Locate and identify every blood parasite.
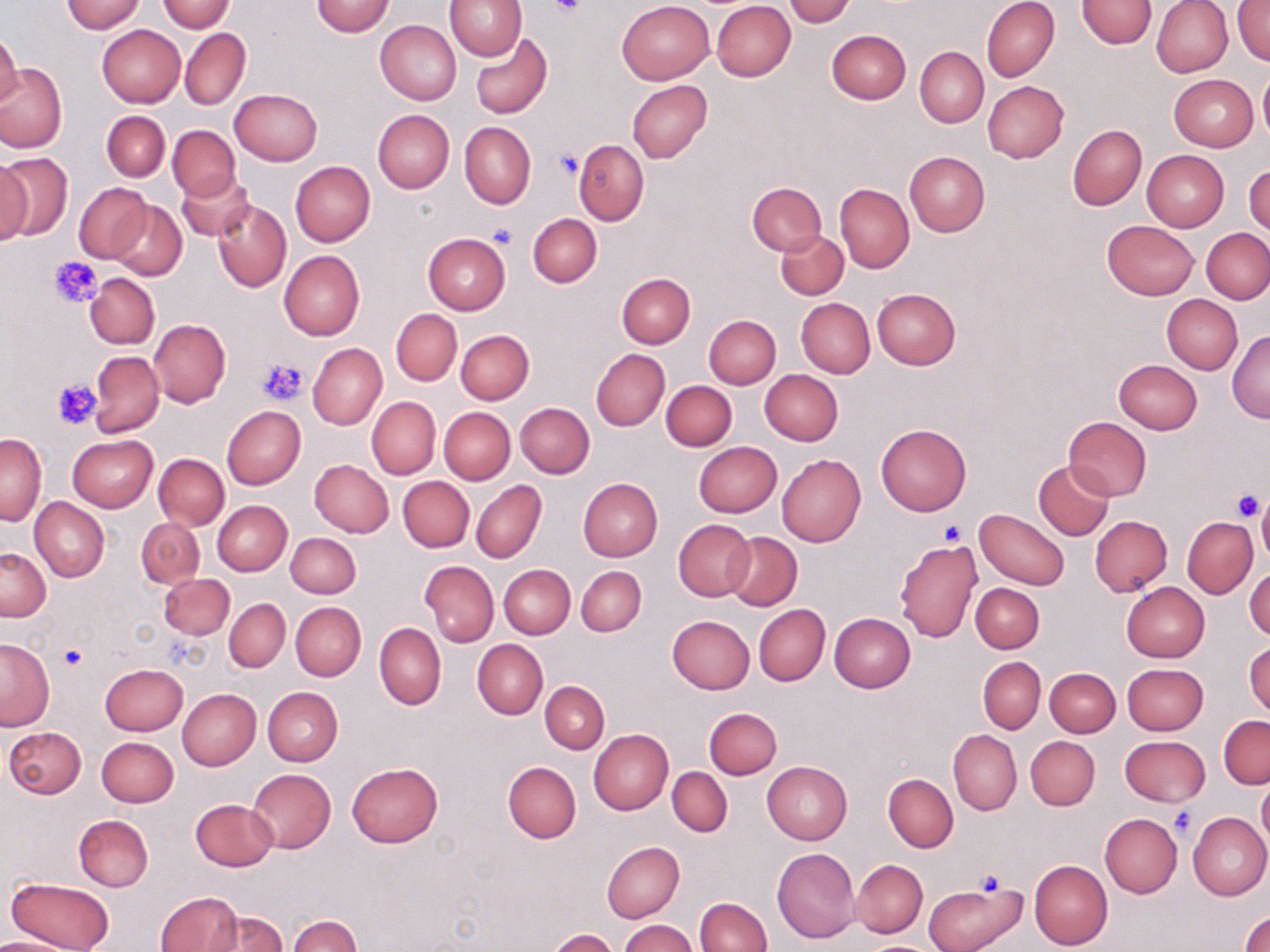

No blood parasites observed.

{
  "slide_level_diagnosis": "negative for blood parasites",
  "preparation": "thin blood film",
  "image_size": "1270×952 pixels",
  "magnification": "1000x",
  "field_of_view": "single",
  "uninfected_red_blood_cell_locations": "approximate bounding boxes as [x1, y1, x2, y2] in pixels: [60, 0, 146, 33], [156, 0, 234, 33], [445, 0, 526, 60], [785, 0, 854, 27], [982, 0, 1059, 82], [1075, 0, 1156, 48], [1151, 0, 1234, 78], [311, 1, 394, 36], [616, 1, 714, 85], [711, 1, 796, 82], [1233, 1, 1270, 65], [375, 20, 461, 105], [97, 25, 185, 106], [181, 27, 251, 110], [827, 30, 910, 105], [0, 32, 23, 109], [469, 32, 552, 120], [915, 47, 988, 127], [1, 63, 67, 153], [1257, 70, 1270, 146], [1169, 75, 1257, 152], [627, 80, 713, 163], [981, 81, 1069, 163], [230, 89, 321, 166], [372, 110, 454, 193], [102, 111, 169, 182], [460, 121, 536, 209], [1068, 124, 1146, 211], [168, 125, 239, 201], [575, 139, 649, 226], [1142, 150, 1229, 231], [0, 151, 72, 243], [904, 152, 990, 237], [0, 157, 33, 245], [290, 161, 376, 246], [1244, 161, 1269, 236], [178, 172, 255, 241], [747, 182, 826, 256], [74, 183, 153, 262], [835, 183, 914, 273], [211, 199, 291, 293], [109, 201, 187, 280], [528, 214, 602, 287], [1101, 219, 1201, 300], [1203, 228, 1269, 302], [776, 230, 848, 299], [422, 234, 509, 315], [279, 250, 365, 341], [85, 273, 159, 348], [615, 273, 695, 348], [872, 288, 961, 370], [1162, 295, 1242, 375], [796, 298, 875, 377], [391, 310, 461, 384], [704, 314, 781, 388], [149, 319, 230, 407], [1227, 329, 1270, 421], [456, 330, 534, 405], [307, 342, 386, 430], [592, 349, 670, 430], [89, 351, 163, 436], [1114, 359, 1203, 434], [759, 370, 843, 446], [662, 381, 737, 451], [367, 397, 440, 479], [515, 402, 594, 477], [222, 406, 305, 489], [440, 408, 515, 484], [1063, 417, 1152, 500], [876, 425, 971, 516], [0, 434, 46, 525], [69, 435, 158, 512], [693, 441, 782, 518], [154, 453, 229, 529], [776, 454, 866, 547], [310, 460, 394, 537], [1034, 461, 1113, 540], [398, 476, 474, 552], [578, 478, 663, 561], [472, 480, 546, 564], [1257, 496, 1270, 567], [30, 499, 109, 582], [213, 500, 291, 576], [976, 508, 1069, 590], [1089, 515, 1172, 596], [137, 517, 205, 587], [1182, 518, 1257, 598], [673, 520, 755, 602], [723, 532, 802, 611], [285, 533, 361, 598], [894, 540, 982, 642], [0, 547, 50, 621], [420, 561, 498, 645], [1246, 563, 1270, 639], [499, 564, 574, 638], [576, 566, 646, 636], [159, 573, 234, 639], [1121, 581, 1209, 662], [971, 582, 1044, 653], [224, 599, 290, 672], [290, 601, 366, 681], [754, 604, 830, 686], [829, 613, 916, 692], [667, 616, 754, 694], [373, 623, 446, 710], [0, 637, 53, 731], [1245, 638, 1269, 720], [473, 639, 548, 718], [977, 657, 1046, 732], [100, 662, 187, 735], [1121, 663, 1207, 734], [1046, 668, 1121, 737], [541, 681, 609, 753], [264, 687, 343, 766], [178, 688, 260, 770], [704, 707, 782, 779], [1219, 715, 1269, 789], [4, 726, 87, 798], [589, 729, 673, 815], [949, 730, 1021, 815], [1120, 735, 1209, 806], [1026, 736, 1099, 810], [97, 737, 179, 807], [762, 761, 852, 844], [346, 762, 442, 847], [503, 762, 581, 843], [668, 767, 732, 837], [248, 769, 336, 852], [883, 774, 958, 852], [1258, 777, 1270, 849], [190, 798, 278, 871], [1187, 812, 1270, 901], [1100, 813, 1181, 897], [74, 815, 154, 891], [601, 841, 684, 922], [772, 846, 861, 943], [1028, 859, 1112, 950], [851, 860, 927, 938], [5, 876, 114, 952], [926, 880, 1029, 952], [154, 891, 244, 952], [696, 897, 772, 952], [206, 911, 287, 951], [1240, 911, 1270, 952], [288, 914, 360, 951], [619, 919, 698, 952], [549, 928, 617, 951], [0, 934, 79, 951], [863, 942, 934, 952]",
  "modality": "optical microscopy",
  "platelet_locations": "approximate bounding boxes as [x1, y1, x2, y2] in pixels: [550, 0, 588, 17], [554, 148, 584, 179], [492, 224, 517, 248], [50, 254, 102, 308], [258, 355, 308, 405], [52, 380, 101, 430], [1231, 489, 1265, 521], [940, 522, 967, 546], [59, 644, 87, 670], [1168, 808, 1198, 839], [974, 871, 1007, 896]",
  "stain": "May-Grünwald-Giemsa"
}